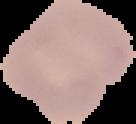
image size = 136×124 pixels
preparation = thin blood film
result = negative for Plasmodium parasites
image type = cell region segmented out of the field of view; surrounding area masked to black